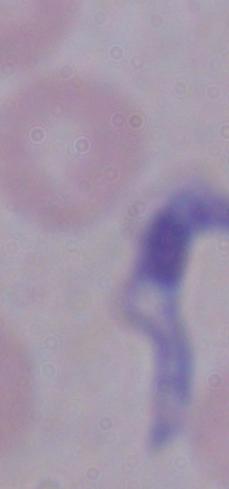

modality = micrograph
magnification = 1000x
identification = trypanosome